Identify the parasite.
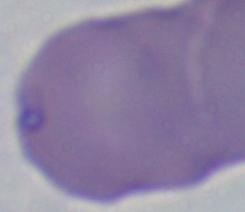
Babesia.

Micrograph. Captured at 1000x magnification.